Describe the morphology of the erythrocytes.
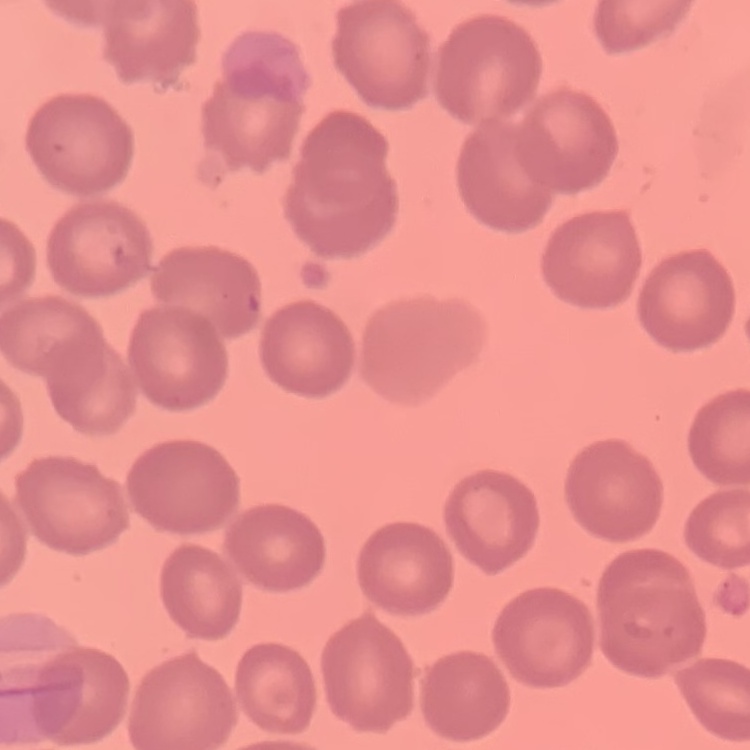
No rouleaux formation.

One tile cut from a larger photomicrograph. Field's or Giemsa stain. Thin peripheral smear.